Report the malaria status of this cell.
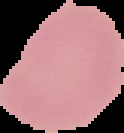
Uninfected.

image size = 124×133 pixels
image type = segmented cell region on a black background
preparation = thin blood film